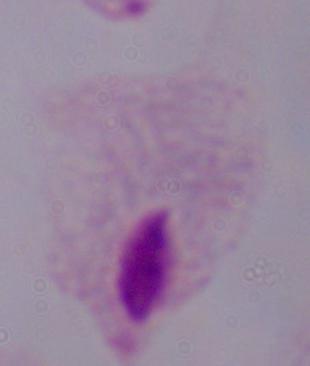 1000x magnification. Photomicrograph. A trichomonad is shown.